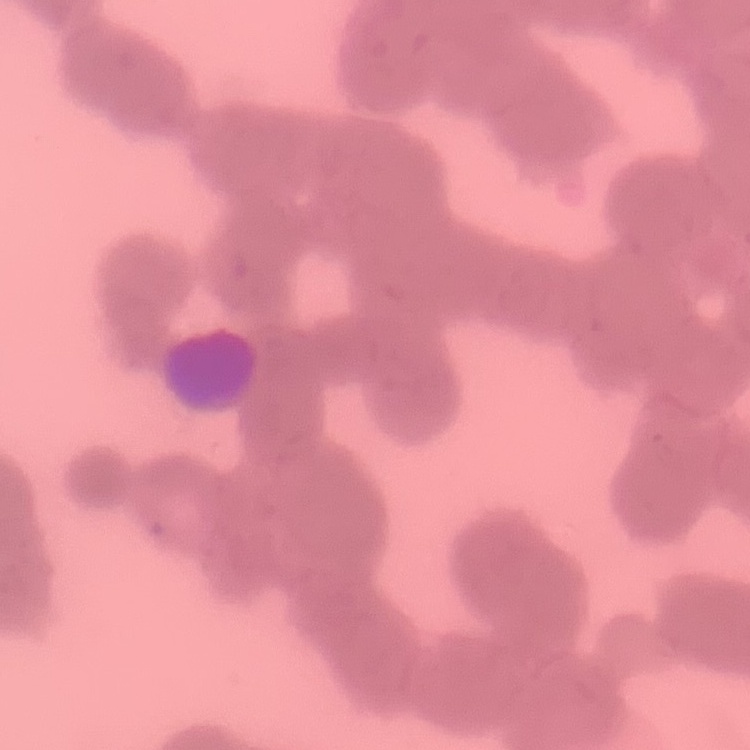 The erythrocytes exhibit rouleaux formation. Thin blood film. Stained with either Field's or Giemsa. One tile cut from a larger photomicrograph.